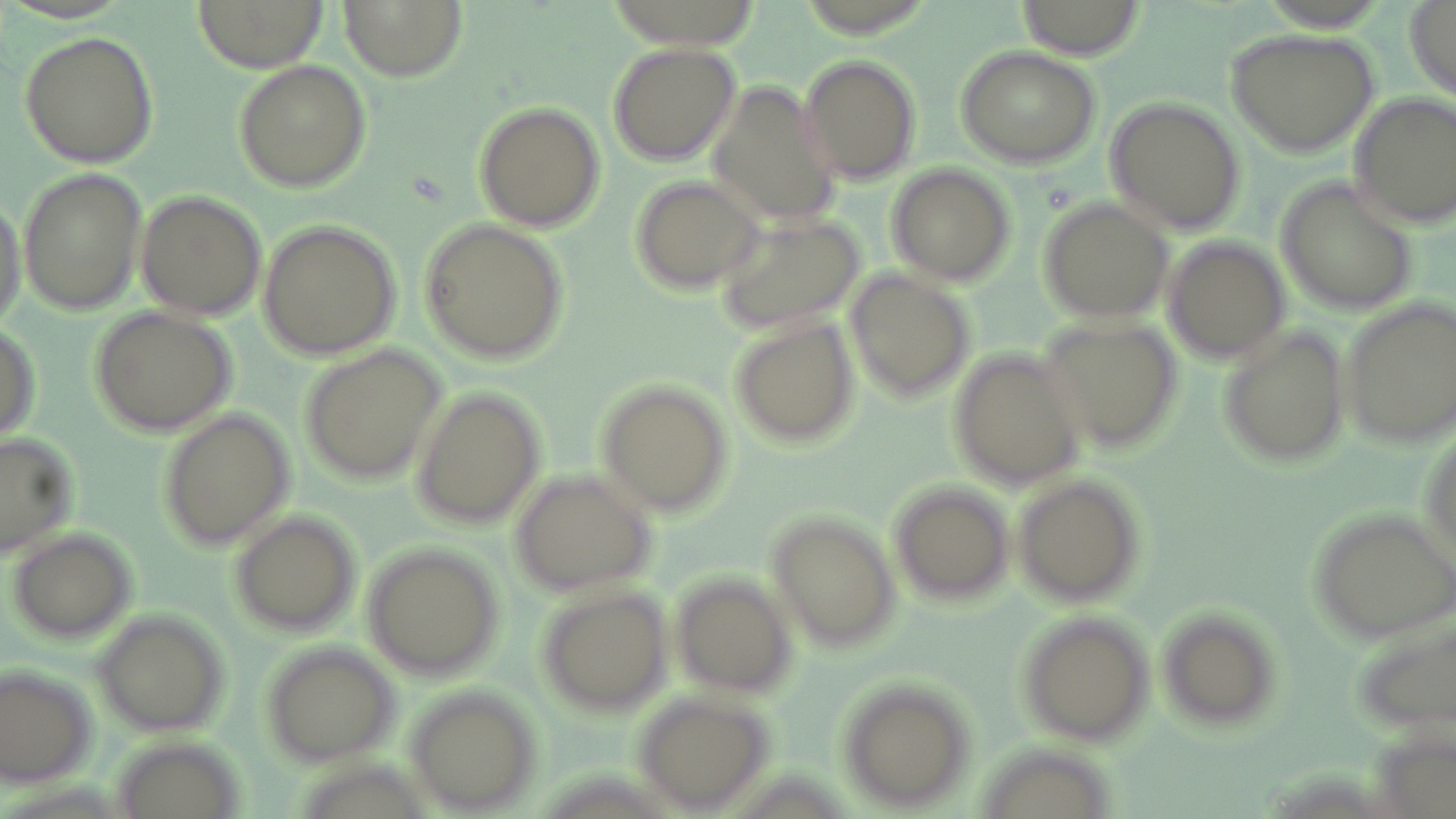
Approximate bounding boxes as named x1/y1/x2/y2 corners in pixels. Uninfected red blood cell locations: (x1=200, y1=0, x2=326, y2=68), (x1=337, y1=0, x2=468, y2=81), (x1=1017, y1=0, x2=1145, y2=61), (x1=1402, y1=3, x2=1456, y2=101), (x1=1227, y1=27, x2=1379, y2=156), (x1=18, y1=30, x2=160, y2=168), (x1=605, y1=40, x2=743, y2=167), (x1=953, y1=45, x2=1102, y2=170), (x1=797, y1=53, x2=922, y2=183), (x1=230, y1=59, x2=373, y2=192), (x1=699, y1=75, x2=848, y2=231), (x1=1347, y1=92, x2=1455, y2=227), (x1=1103, y1=95, x2=1248, y2=233), (x1=471, y1=100, x2=606, y2=231), (x1=885, y1=164, x2=1016, y2=288), (x1=16, y1=167, x2=152, y2=316), (x1=625, y1=173, x2=764, y2=296), (x1=1278, y1=180, x2=1423, y2=313), (x1=0, y1=187, x2=29, y2=333), (x1=134, y1=188, x2=268, y2=323), (x1=1035, y1=194, x2=1175, y2=323), (x1=715, y1=212, x2=865, y2=331), (x1=415, y1=218, x2=572, y2=367), (x1=256, y1=221, x2=402, y2=361), (x1=1162, y1=235, x2=1292, y2=365), (x1=846, y1=267, x2=977, y2=404), (x1=1336, y1=298, x2=1455, y2=447), (x1=88, y1=304, x2=236, y2=436), (x1=1035, y1=313, x2=1183, y2=452), (x1=724, y1=314, x2=861, y2=449), (x1=1218, y1=326, x2=1352, y2=471), (x1=296, y1=339, x2=449, y2=488), (x1=947, y1=347, x2=1088, y2=490), (x1=595, y1=378, x2=734, y2=518), (x1=407, y1=385, x2=547, y2=528), (x1=156, y1=408, x2=295, y2=548), (x1=0, y1=432, x2=79, y2=554), (x1=508, y1=468, x2=658, y2=597), (x1=1010, y1=474, x2=1149, y2=608), (x1=886, y1=479, x2=1017, y2=608), (x1=1304, y1=505, x2=1456, y2=644), (x1=230, y1=512, x2=360, y2=635), (x1=765, y1=512, x2=901, y2=654), (x1=6, y1=528, x2=138, y2=640), (x1=360, y1=542, x2=506, y2=680), (x1=673, y1=574, x2=799, y2=697), (x1=532, y1=586, x2=672, y2=715), (x1=1152, y1=604, x2=1285, y2=733), (x1=90, y1=608, x2=231, y2=738), (x1=1011, y1=608, x2=1157, y2=747), (x1=257, y1=642, x2=404, y2=766), (x1=1, y1=662, x2=96, y2=789), (x1=832, y1=679, x2=976, y2=812), (x1=401, y1=684, x2=545, y2=812), (x1=632, y1=689, x2=774, y2=811). Slide-level diagnosis: Plasmodium ovale. Thin blood smear. May-Grünwald-Giemsa stain. Image is 1456×819 pixels. Single field of view. Light microscopy. 1000x magnification.